Assess this cell for malaria.
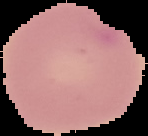
It is parasitized.

Cell region segmented out of the field of view; the surrounding area is masked to black. From a thin blood film. Image is 148×136 pixels.